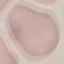

Summary:
  - Result: no malaria parasites seen
  - Stain: Giemsa
  - Preparation: thin smear
  - Image type: cell patch, automatically extracted from a larger field of view and resized to 64 × 64 pixels
  - Capture: smartphone camera at the microscope eyepiece